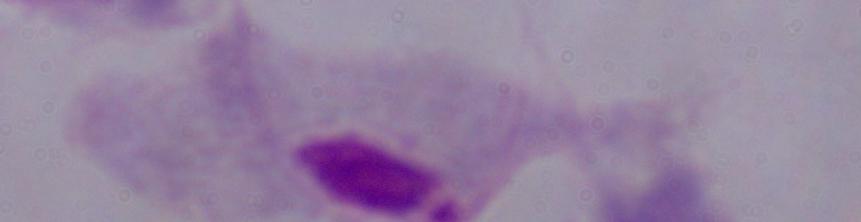

modality = micrograph
magnification = 1000x
identification = trichomonad